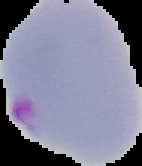
Summary:
  - Image size: 142×166 pixels
  - Malaria status: parasitized
  - Preparation: thin blood film
  - Image type: segmented cell region on a black background